Report the malaria status of this cell.
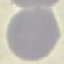

It is uninfected.

Photographed with a smartphone camera at the microscope eyepiece. Thin blood smear. Cell patch, automatically extracted from a larger field of view and resized to 64 × 64 pixels. Giemsa stain.